State which cell type is depicted.
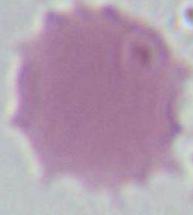
This is an erythrocyte.

Photomicrograph. Captured at 1000x magnification.